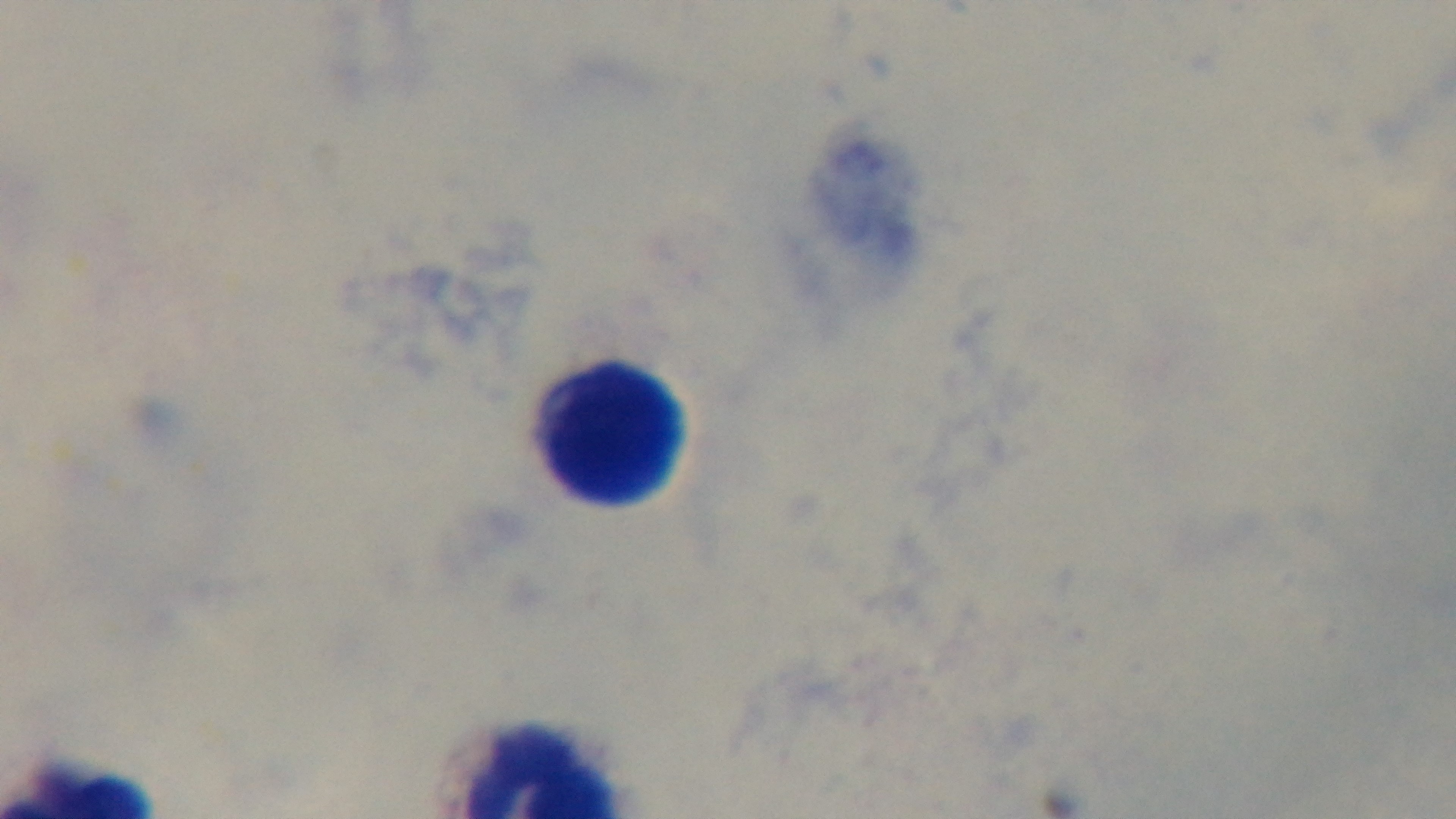

Mounted 4K digital camera. Light microscopy. Giemsa stain. One field from the slide. Malaria status: uninfected. 100x oil-immersion objective. Preparation: thick.